Assess the morphology of the erythrocytes.
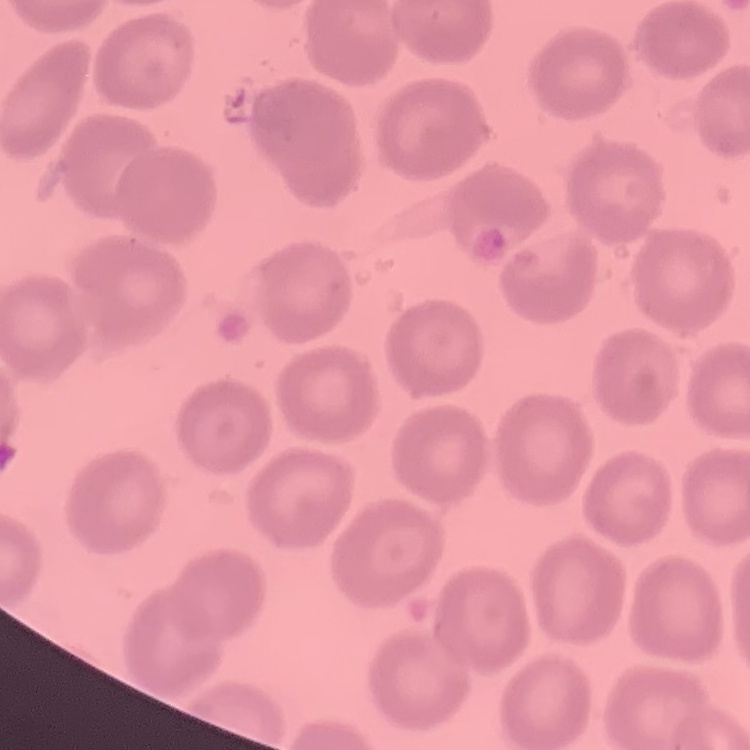

No rouleaux formation.

{
  "stain": "Field's or Giemsa",
  "preparation": "thin blood smear",
  "image_type": "square crop of a larger photomicrograph"
}